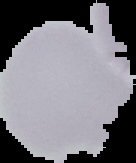
result = no malaria parasites seen
image size = 136×163 pixels
image type = segmented cell region on a black background
preparation = thin blood film